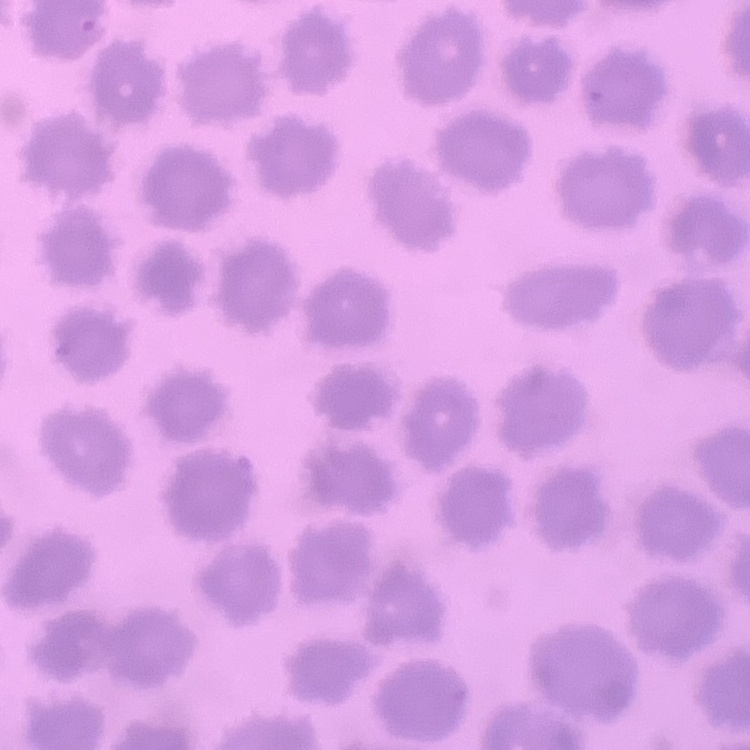
erythrocyte_morphology: no rouleaux formation
preparation: thin blood film
image_type: one tile cut from a larger photomicrograph
stain: Field's or Giemsa